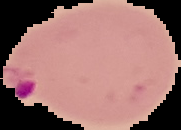
Summary:
  - Preparation: thin blood smear
  - Image type: segmented cell region on a black background
  - Malaria status: parasitized
  - Image size: 181×130 pixels